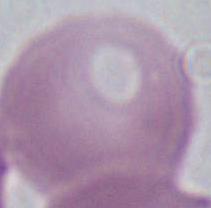

An erythrocyte is seen. Captured at 1000x magnification. Micrograph.